Which red blood cells are P. falciparum-infected, and which are of indeterminate infection status?
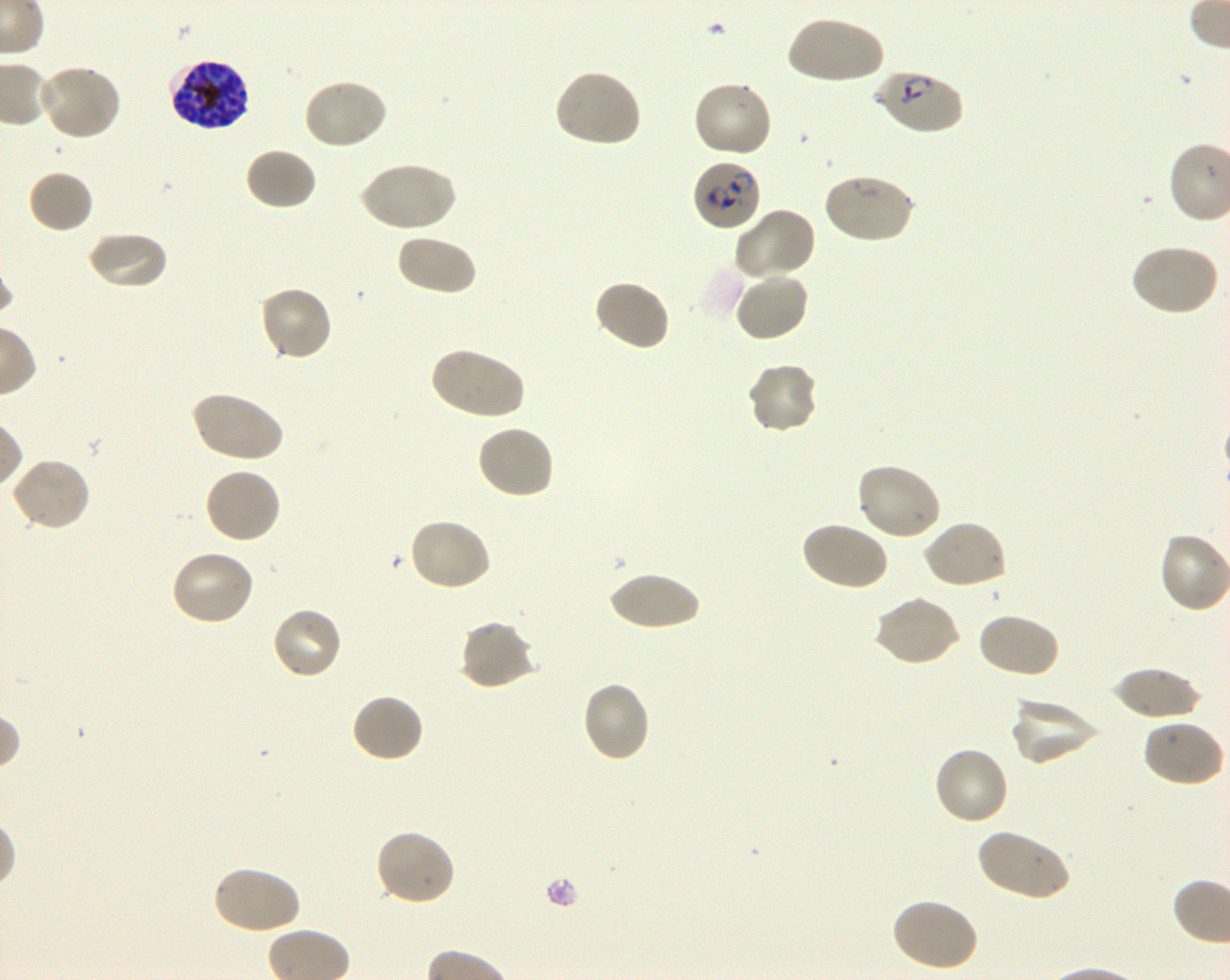

Approximate bounding boxes as [x1, y1, x2, y2] in pixels. Not every red blood cell is marked. A life-cycle stage — or a range of stages, where the recorded stages span more than one — follows each staged infected red blood cell.
Infected red blood cells: [169, 58, 251, 131] schizont; [874, 69, 965, 136] early ring to early trophozoite; [692, 159, 762, 231] ring.
No red blood cells of indeterminate infection status observed.

Summary:
  - Locations of uninfected red blood cells: [787, 15, 885, 86], [37, 63, 122, 141], [553, 69, 642, 149], [303, 77, 389, 151], [692, 80, 773, 159], [244, 146, 318, 212], [359, 161, 455, 233], [27, 169, 95, 234], [821, 173, 915, 245], [733, 207, 817, 282], [87, 231, 168, 291], [395, 233, 477, 296], [1129, 243, 1221, 317], [733, 270, 810, 342], [592, 279, 672, 352], [258, 285, 334, 362], [428, 346, 525, 421], [746, 360, 819, 434], [190, 391, 284, 465], [476, 424, 555, 501], [10, 456, 92, 532], [855, 463, 943, 543], [203, 465, 282, 545], [407, 517, 493, 591], [922, 519, 1008, 590], [800, 520, 889, 591], [168, 549, 256, 627], [607, 570, 703, 630], [872, 594, 960, 667], [270, 606, 345, 680], [976, 612, 1061, 679], [458, 619, 537, 691], [1111, 667, 1203, 720], [581, 680, 651, 764], [350, 693, 425, 765], [1009, 695, 1102, 766], [1141, 718, 1225, 788], [933, 746, 1011, 827], [976, 827, 1071, 901], [375, 828, 457, 906], [211, 865, 301, 935], [891, 897, 979, 973]
  - Life-cycle stages observed: ring, schizont
  - Image size: 1230×980 pixels
  - Donor blood group: O+
  - Culture: shaking in-vitro P. falciparum strain 3D7
  - Stain: Giemsa
  - Objective: 100x, oil immersion, numerical aperture 1.30
  - Preparation: thin blood smear
  - Field of view: single